Point out each Plasmodium parasite and each leukocyte.
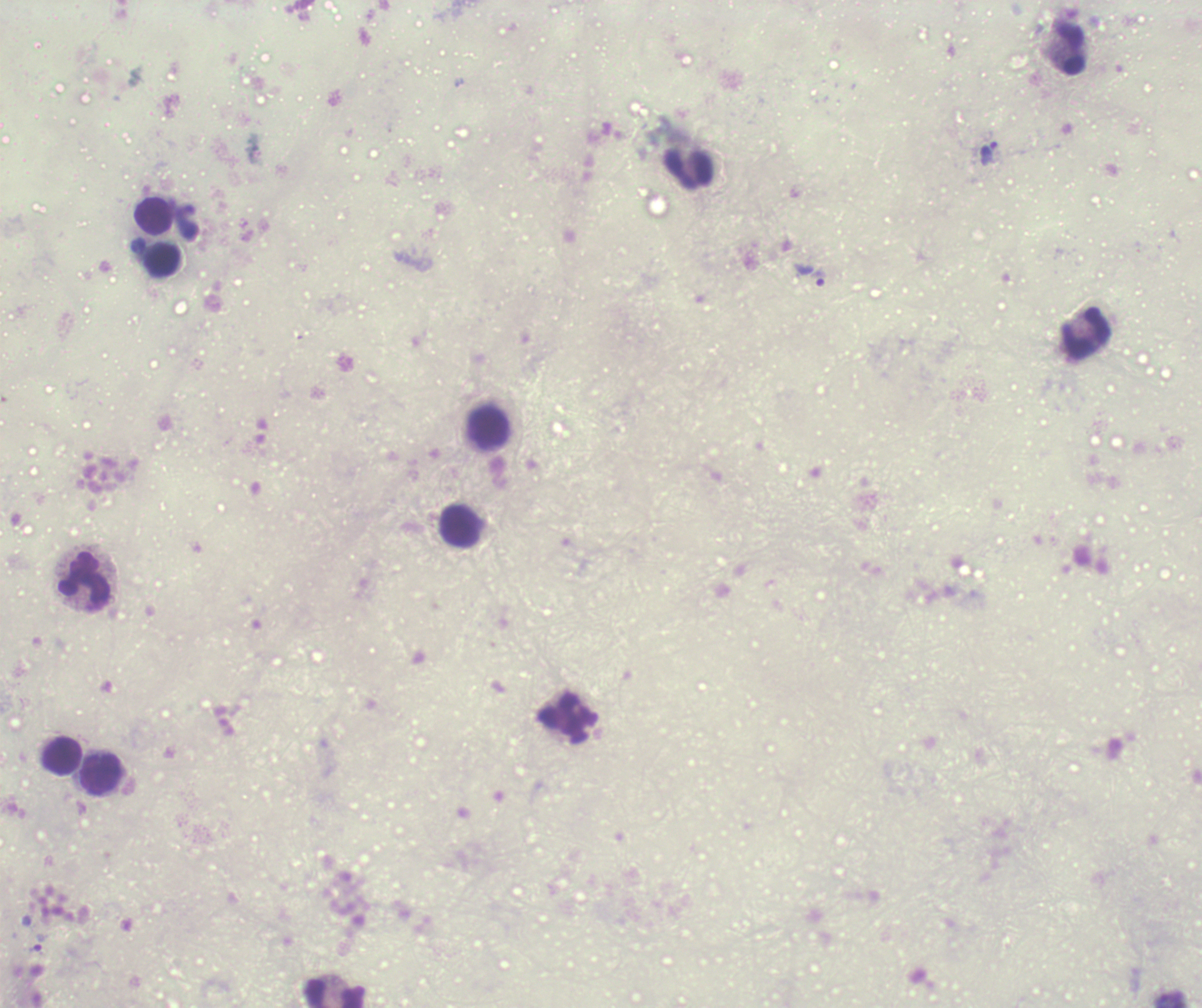
Approximate centers as (x, y) in pixels.
Trophozoites: (989, 154), (820, 278), (39, 942).
No schizont or gametocyte forms observed.
Leukocytes: (1068, 49), (688, 168), (152, 216), (161, 259), (1086, 334), (489, 426), (460, 526), (85, 578), (568, 717), (62, 756), (101, 773), (336, 994).

Summary:
  - Stain: Romanowsky
  - Background quality: poor
  - Magnification: 100x
  - Context: previously used in a real diagnosis
  - Coloration quality: bad
  - Image size: 1202×1008 pixels
  - Preparation: thick blood film
  - Field of view: single